Draw a bounding box around every artifact (stain precipitate or debris).
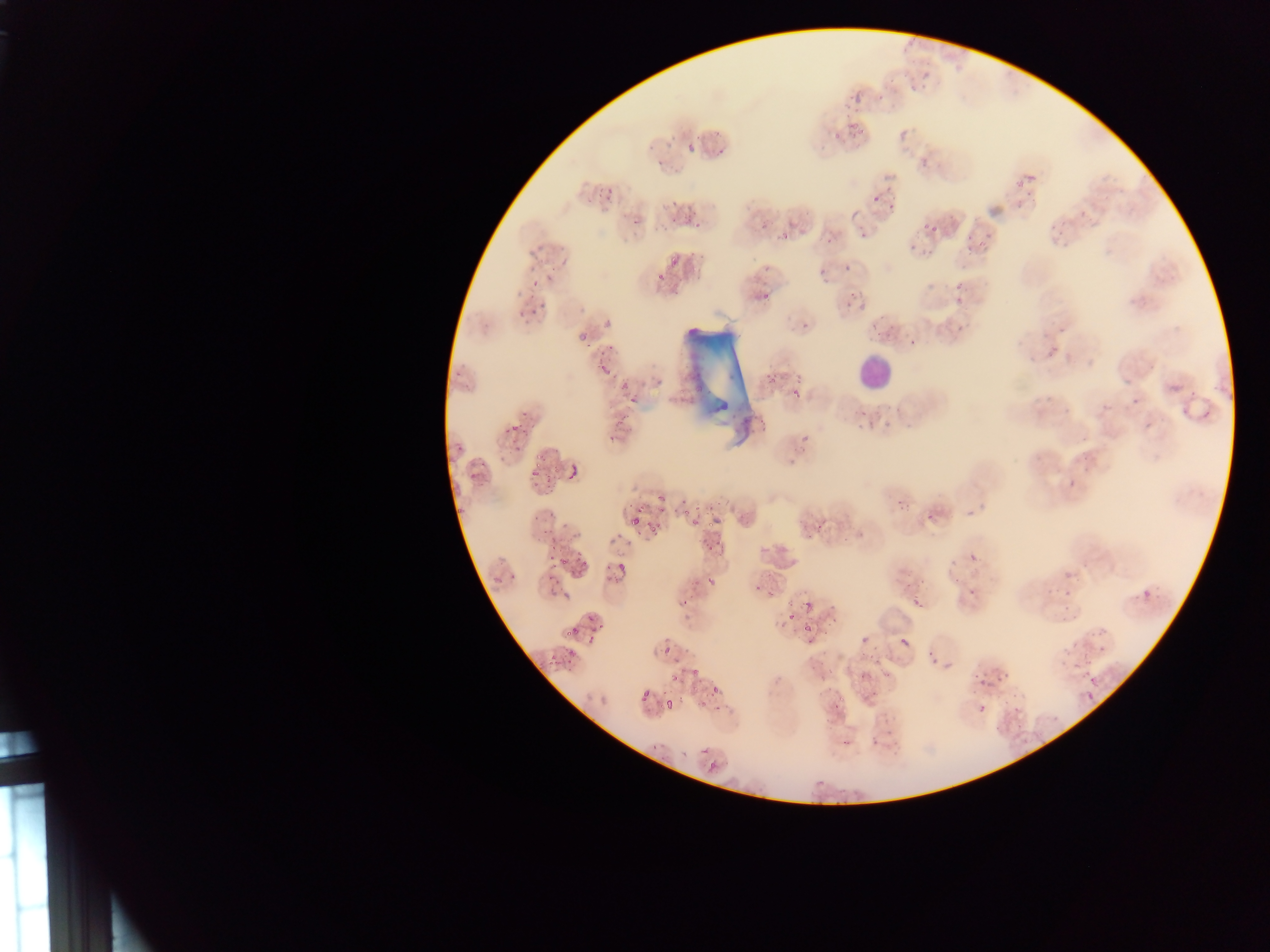

Approximate bounding boxes as (left, top, right, bottom) in pixels.
Artifacts (stain precipitate or debris): (679, 318, 749, 440).

{
  "image_size": "1270×952 pixels",
  "preparation": "thin blood film",
  "capture": "mobile-phone photograph through a microscope",
  "leukocyte_locations": "approximate bounding boxes as (left, top, right, bottom) in pixels: (854, 352, 894, 392)",
  "country": "Ghana",
  "field_of_view": "single",
  "plasmodium_parasite_locations": "approximate bounding boxes as (left, top, right, bottom) in pixels: (898, 73, 920, 94), (846, 79, 864, 98), (877, 89, 888, 107), (849, 115, 867, 137), (899, 126, 911, 141), (705, 129, 719, 139), (831, 129, 841, 143), (710, 139, 727, 158), (687, 143, 696, 153), (648, 155, 666, 170), (918, 156, 931, 169), (1015, 165, 1042, 186), (867, 183, 895, 204), (594, 185, 615, 204), (1013, 193, 1028, 209), (668, 197, 680, 216), (887, 201, 896, 214), (677, 208, 700, 228), (630, 218, 643, 229), (911, 227, 946, 261), (776, 228, 796, 242), (970, 240, 980, 252), (662, 254, 678, 275), (843, 258, 860, 272), (550, 265, 557, 275), (525, 271, 540, 292), (650, 271, 664, 286), (950, 282, 962, 291), (761, 288, 772, 300), (833, 288, 866, 312), (519, 290, 552, 316), (945, 295, 965, 308), (876, 309, 889, 332), (603, 316, 613, 330), (577, 326, 594, 342), (906, 335, 921, 346), (596, 345, 617, 356), (456, 361, 471, 373), (598, 362, 611, 374), (766, 368, 777, 380), (618, 376, 632, 393), (789, 385, 808, 403), (628, 393, 643, 405), (856, 405, 875, 419), (616, 410, 627, 424), (507, 423, 523, 435), (607, 428, 621, 446), (452, 438, 469, 459), (506, 443, 528, 456), (527, 445, 552, 478), (469, 453, 489, 479), (571, 460, 583, 479), (539, 474, 553, 492), (689, 492, 726, 533), (643, 493, 669, 517), (453, 497, 466, 521), (932, 512, 941, 521), (630, 515, 642, 526), (804, 521, 825, 540), (646, 522, 663, 539), (542, 524, 558, 546), (707, 540, 723, 550), (567, 552, 587, 573), (609, 553, 630, 578), (544, 560, 558, 584), (949, 566, 969, 586), (492, 568, 513, 586), (706, 577, 717, 594), (1063, 585, 1077, 606), (972, 587, 980, 594), (1141, 589, 1151, 599), (907, 590, 926, 603), (679, 597, 693, 607), (794, 604, 818, 640), (568, 614, 597, 637), (1096, 636, 1114, 654), (901, 638, 909, 646), (556, 645, 579, 670), (665, 649, 673, 667), (926, 652, 944, 665), (812, 663, 838, 680), (688, 664, 701, 689), (861, 668, 875, 679), (670, 672, 689, 685), (974, 672, 1006, 691), (1085, 674, 1104, 689), (710, 686, 720, 695), (836, 688, 858, 706), (641, 691, 650, 701), (1086, 693, 1095, 708), (664, 698, 675, 708), (697, 699, 707, 710), (699, 747, 708, 754), (707, 763, 716, 772) | approximate (x, y) pixel centers of objects too small to bound: (899, 507)"
}